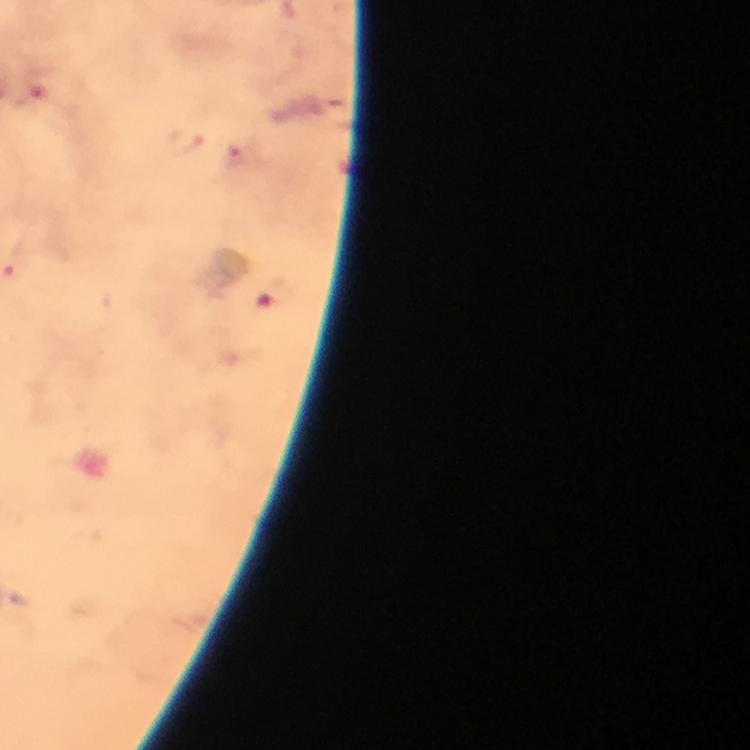
Approximate centers as [x, y] in pixels.
Summary:
  - Plasmodium parasite locations: [40, 85], [186, 140], [240, 157], [15, 270], [273, 296]
  - Cropped from: one field of view
  - Magnification: 100x
  - Preparation: thick smear
  - Capture: smartphone photograph through a microscope
  - Stain: Giemsa
  - Immersion oil: used
  - Image size: 750×750 pixels
  - Context: from a malaria diagnostic workup